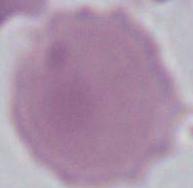 1000x magnification. Micrograph. A red blood cell is seen.